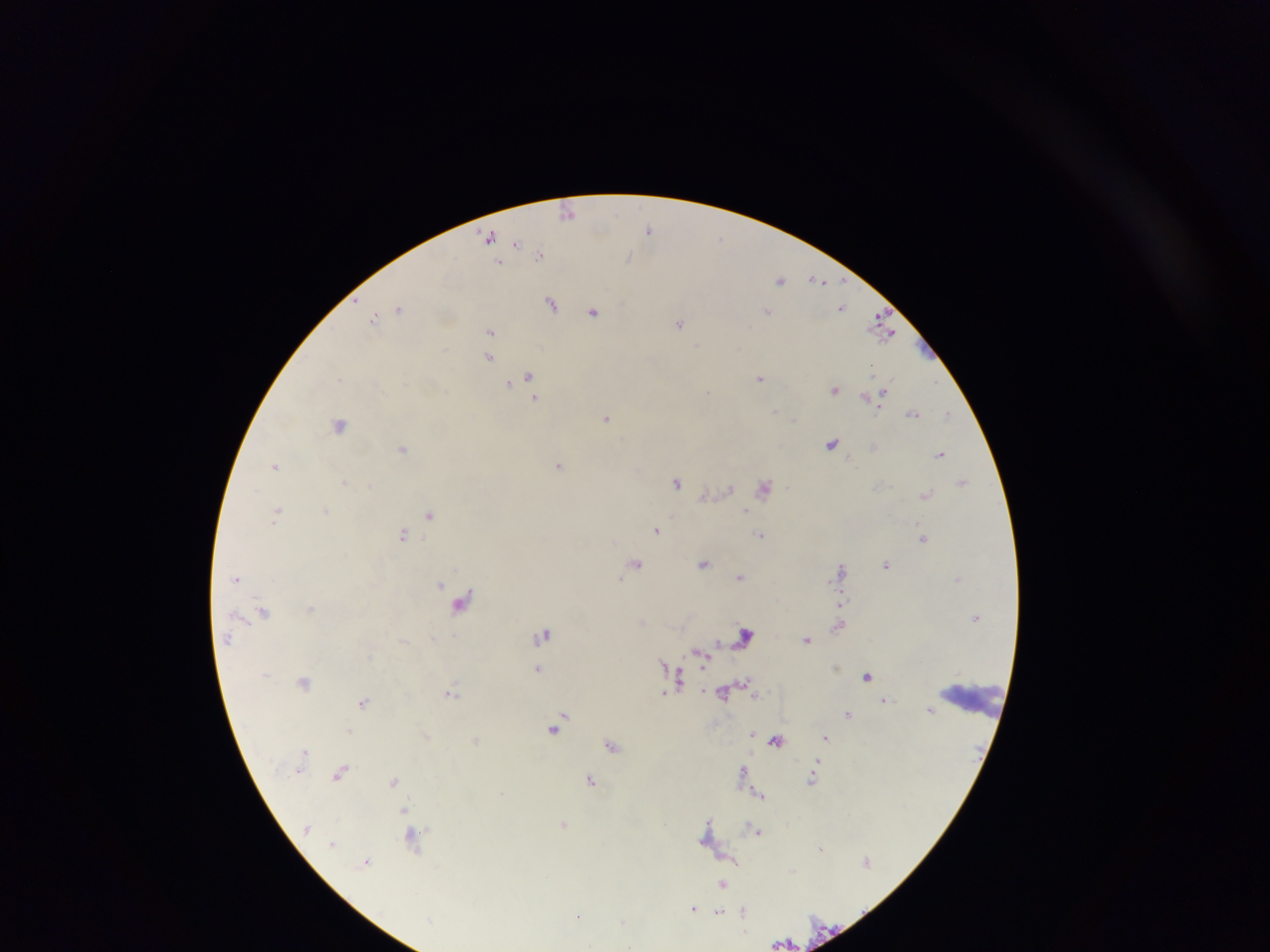

Approximate centers as x y in pixels.
Summary:
  - Leukocyte locations: 976 696
  - Plasmodium parasite locations: 568 213; 649 229; 489 236; 721 238; 516 242; 540 254; 629 258; 499 262; 780 279; 817 280; 552 302; 841 306; 399 308; 768 311; 594 312; 374 318; 880 319; 679 322; 490 331; 885 333; 697 345; 488 357; 873 370; 529 377; 760 378; 340 379; 508 383; 834 389; 708 392; 880 396; 866 397; 535 398; 775 412; 912 413; 947 413; 607 418; 794 419; 340 424; 831 443; 873 447; 402 449; 941 454; 275 465; 559 465; 676 481; 344 482; 963 482; 370 486; 765 487; 729 488; 926 495; 325 510; 745 510; 277 512; 429 514; 658 529; 403 535; 760 536; 923 538; 705 563; 635 564; 886 565; 841 568; 740 577; 236 578; 620 579; 440 584; 462 601; 311 609; 264 612; 643 622; 839 625; 543 634; 745 634; 227 639; 807 639; 717 642; 699 655; 538 669; 867 676; 678 678; 746 681; 304 683; 451 692; 723 693; 664 694; 756 695; 885 700; 363 701; 930 710; 848 714; 563 717; 555 727; 350 731; 752 732; 427 736; 825 737; 475 740; 776 741; 611 745; 304 751; 743 770; 341 771; 812 779; 394 780; 590 781; 759 795; 403 811; 709 822; 666 823; 565 824; 709 827; 757 832; 414 838; 332 844; 820 848; 734 860; 366 862; 722 885; 693 908; 744 912; 719 913; 579 916; 623 922
  - Capture: mobile-phone photograph through a microscope
  - Field of view: single
  - Image size: 1270×952 pixels
  - Preparation: thick blood film
  - Country: Ghana